Point out each leukocyte.
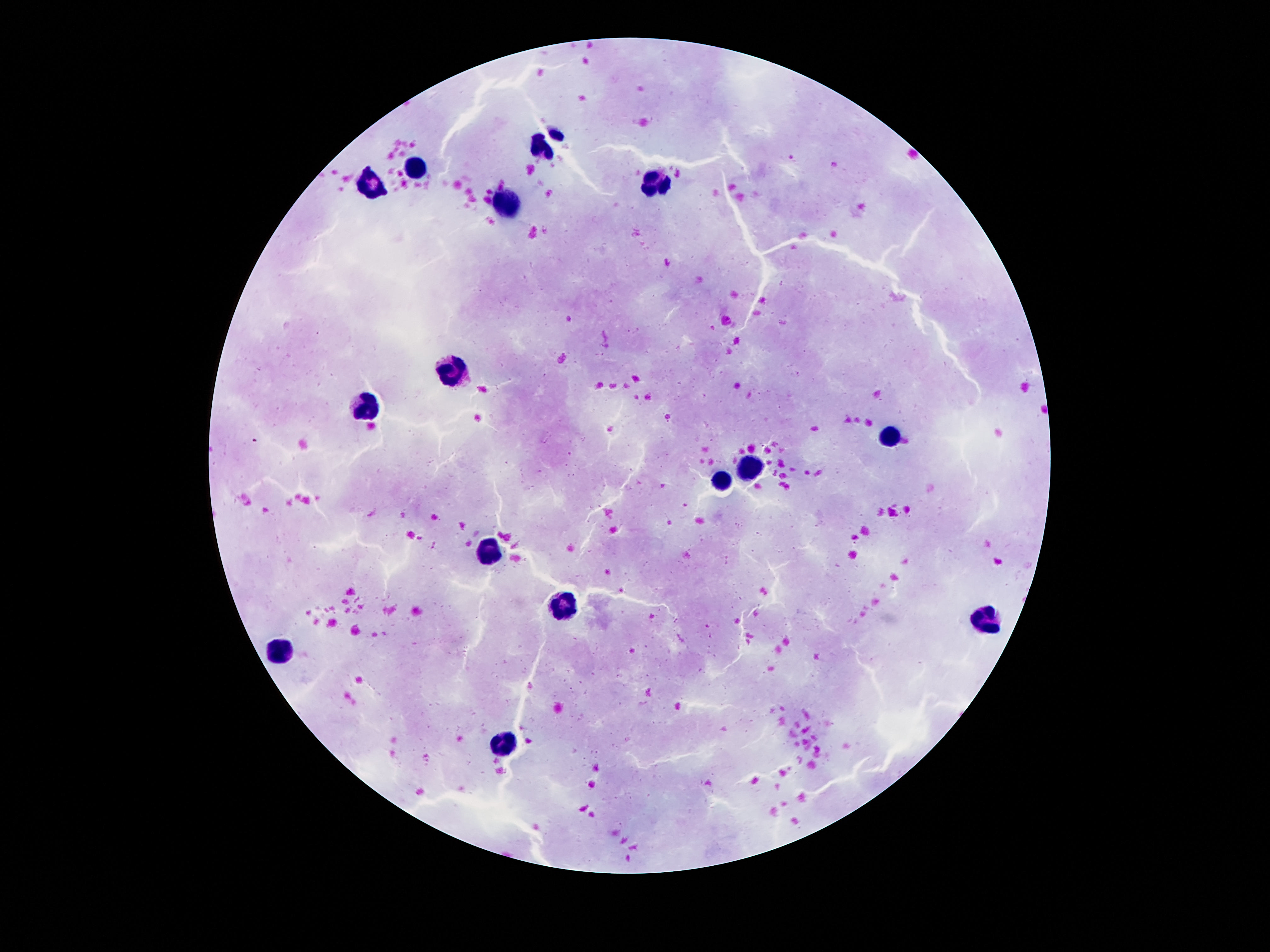

Approximate centers as {x, y} in pixels.
Leukocytes: {416, 170}, {371, 182}, {654, 184}, {509, 203}, {457, 369}, {366, 408}, {892, 438}, {751, 469}, {717, 483}, {488, 550}, {563, 605}, {985, 621}, {280, 650}, {504, 744}.

Patient malaria status: negative. Image is 1270×952 pixels. Giemsa-stained preparation. 100x magnification. Smartphone photograph taken through the microscope eyepiece. Thick peripheral-blood smear. Single field of view.